Report the malaria status of this cell.
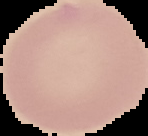
It is uninfected.

{
  "image_size": "148×136 pixels",
  "preparation": "thin blood smear",
  "image_type": "segmented cell region on a black background"
}